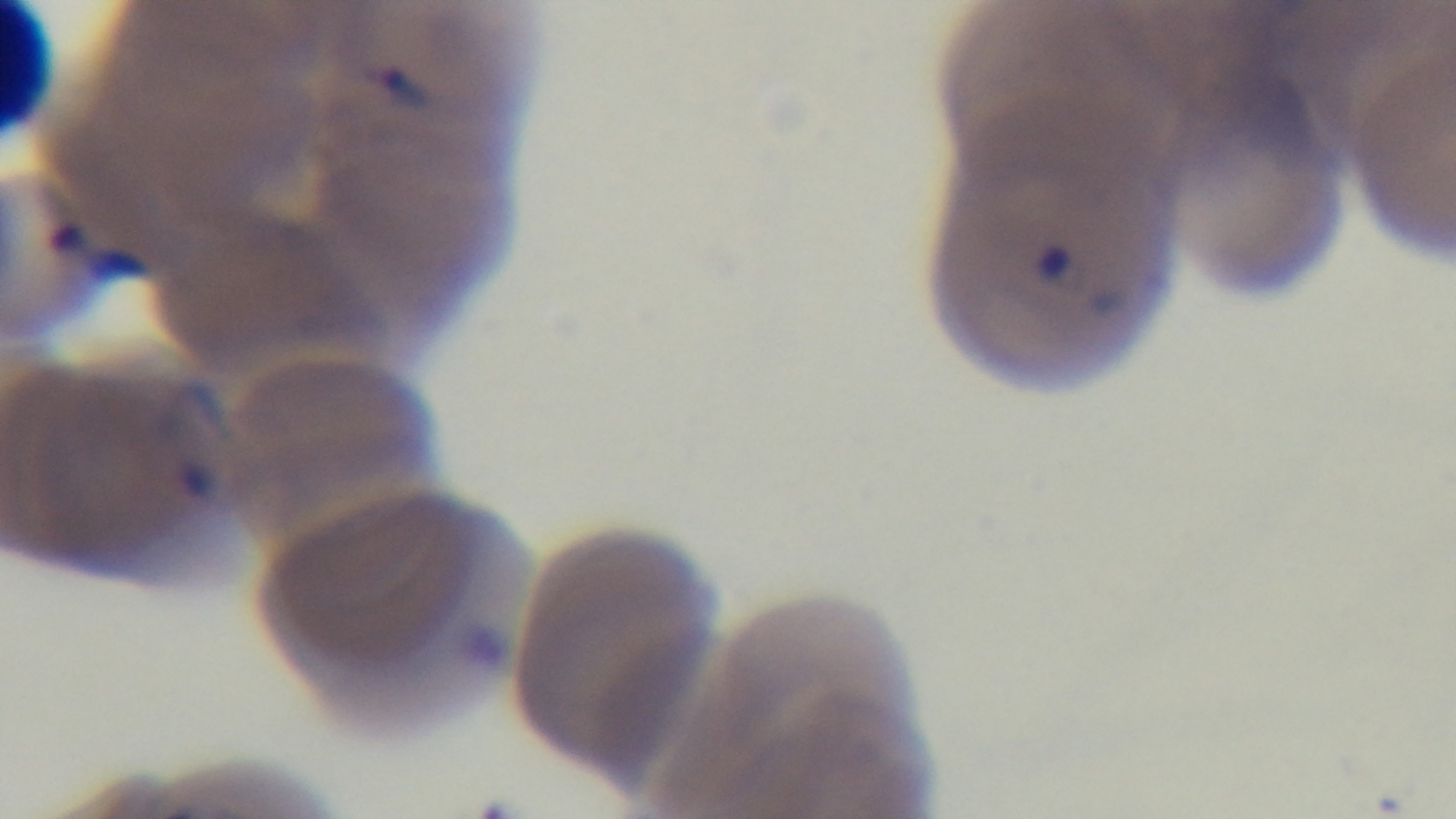
Summary:
  - Malaria status: infected
  - Preparation: thin smear
  - Objective: 100x oil immersion
  - Stain: Giemsa
  - Field of view: one from the slide
  - Modality: light microscopy
  - Capture: mounted 4K digital camera